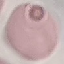
malaria status = uninfected
stain = Giemsa
preparation = thin blood smear
capture = smartphone camera at the microscope eyepiece
image type = cell patch, automatically extracted from a larger field of view and resized to 64 × 64 pixels